State which parasite is depicted.
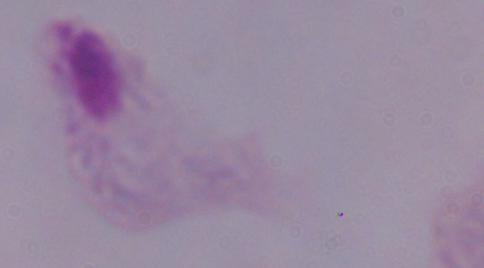
A trichomonad.

modality: micrograph
magnification: 1000x